Classify this cell by malaria status.
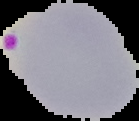

It is parasitized.

From a thin blood smear. Image is 139×121 pixels. Segmented cell region on a black background.